Comment on the morphology of the erythrocytes.
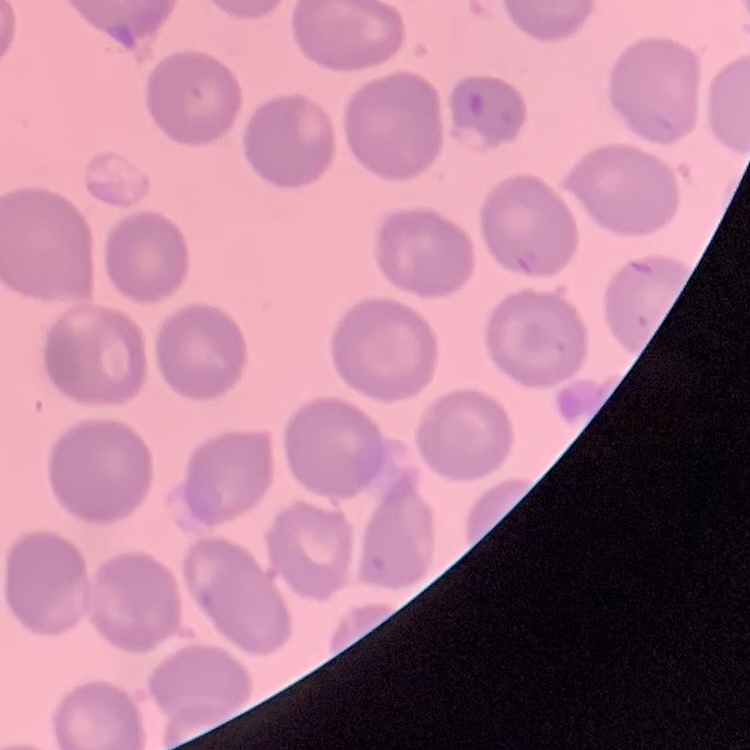

No rouleaux formation.

Stained with either Field's or Giemsa. Square crop of a larger photomicrograph. Thin blood film.